Assess this cell for malaria.
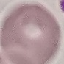

Uninfected.

Summary:
  - Capture: smartphone through the microscope eyepiece
  - Preparation: thin blood smear
  - Image type: cell patch, automatically extracted from a larger field of view and resized to 64 × 64 pixels
  - Stain: Giemsa